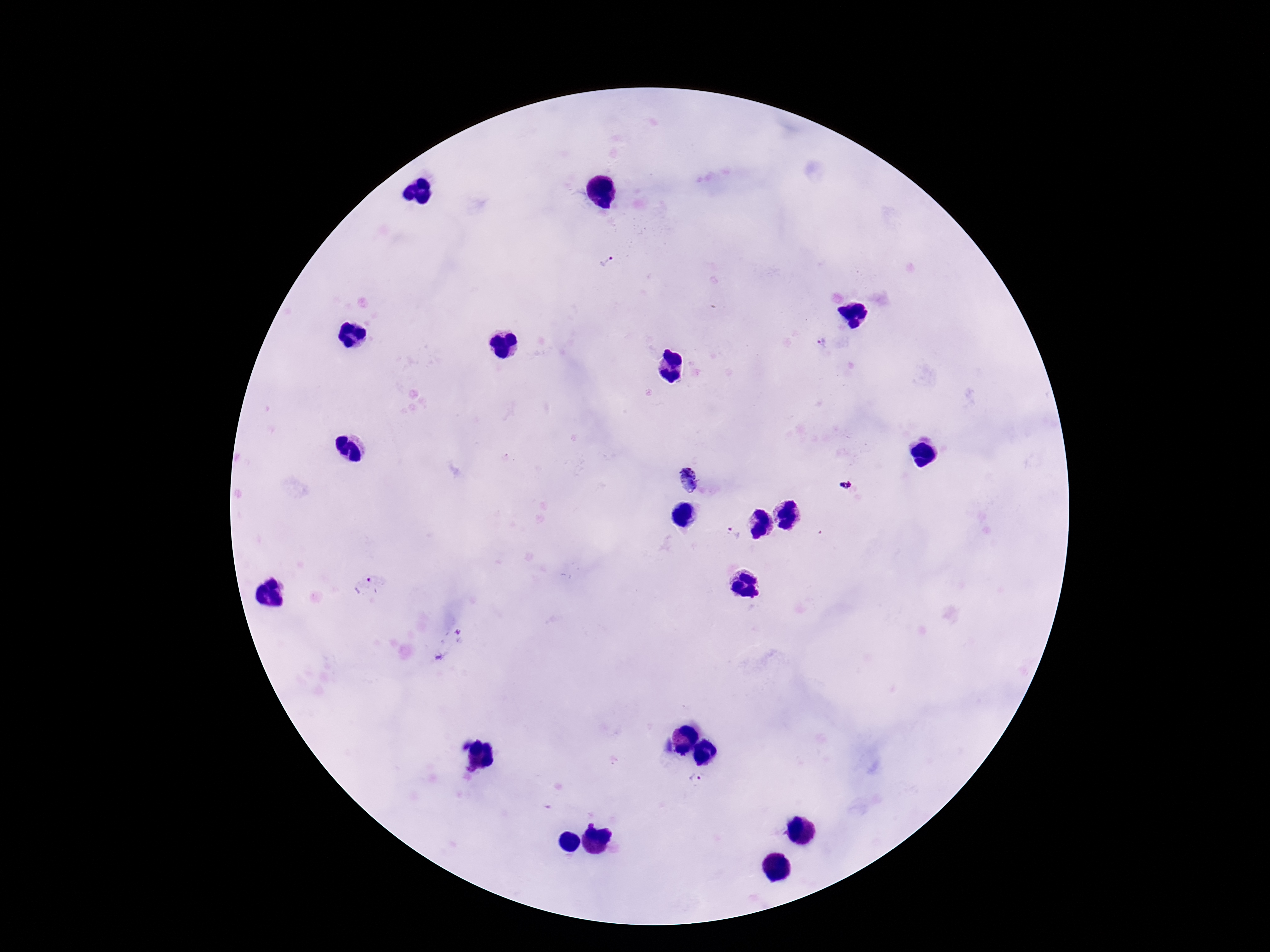
Approximate centers as [x, y] in pixels.
Summary:
  - Plasmodium parasite locations: [607, 259], [821, 341], [688, 480], [733, 533], [694, 781]
  - Image size: 1270×952 pixels
  - Capture: smartphone camera through the microscope eyepiece
  - Field of view: single
  - Stain: Giemsa
  - Preparation: thick blood smear
  - Patient malaria status: infected
  - Magnification: 100x